Name the parasite shown.
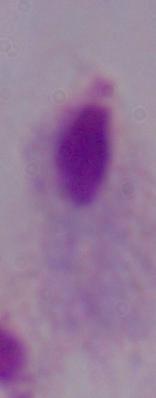

A trichomonad.

Captured at 1000x magnification. Photomicrograph.